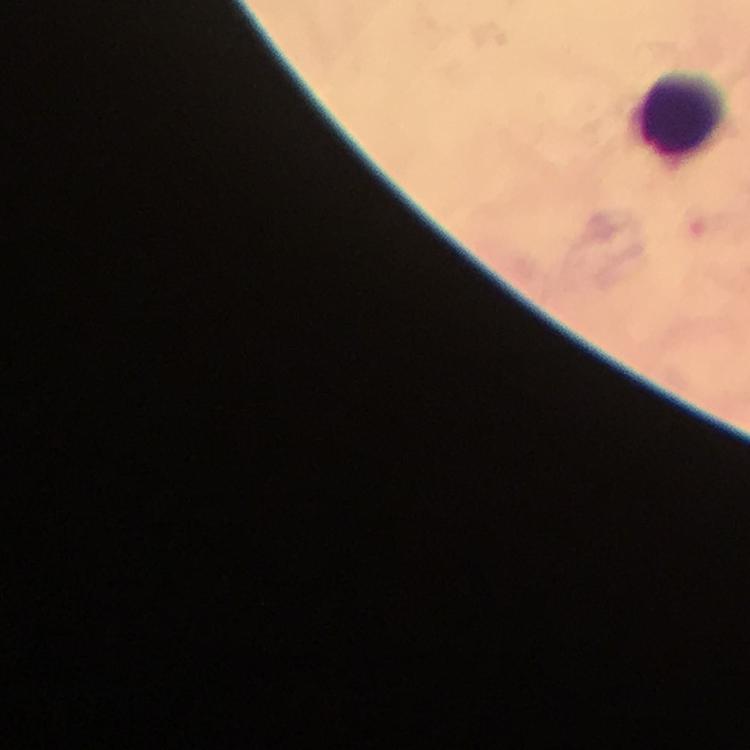

{
  "magnification": "100x",
  "capture": "smartphone mounted on the microscope",
  "stain": "Giemsa",
  "leukocyte_locations": "approximate centers as (x, y) in pixels: (681, 116)",
  "immersion_oil": "used",
  "cropped_from": "one field of view",
  "context": "from a diagnostic examination for malaria",
  "image_size": "750×750 pixels",
  "plasmodium_parasites": "none seen",
  "preparation": "thick blood smear"
}